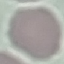 Result: no malaria parasites seen. Automatically extracted cell patch, resized to 64 × 64 pixels. Photographed with a smartphone camera at the microscope eyepiece. Thin smear of blood. Giemsa-stained preparation.